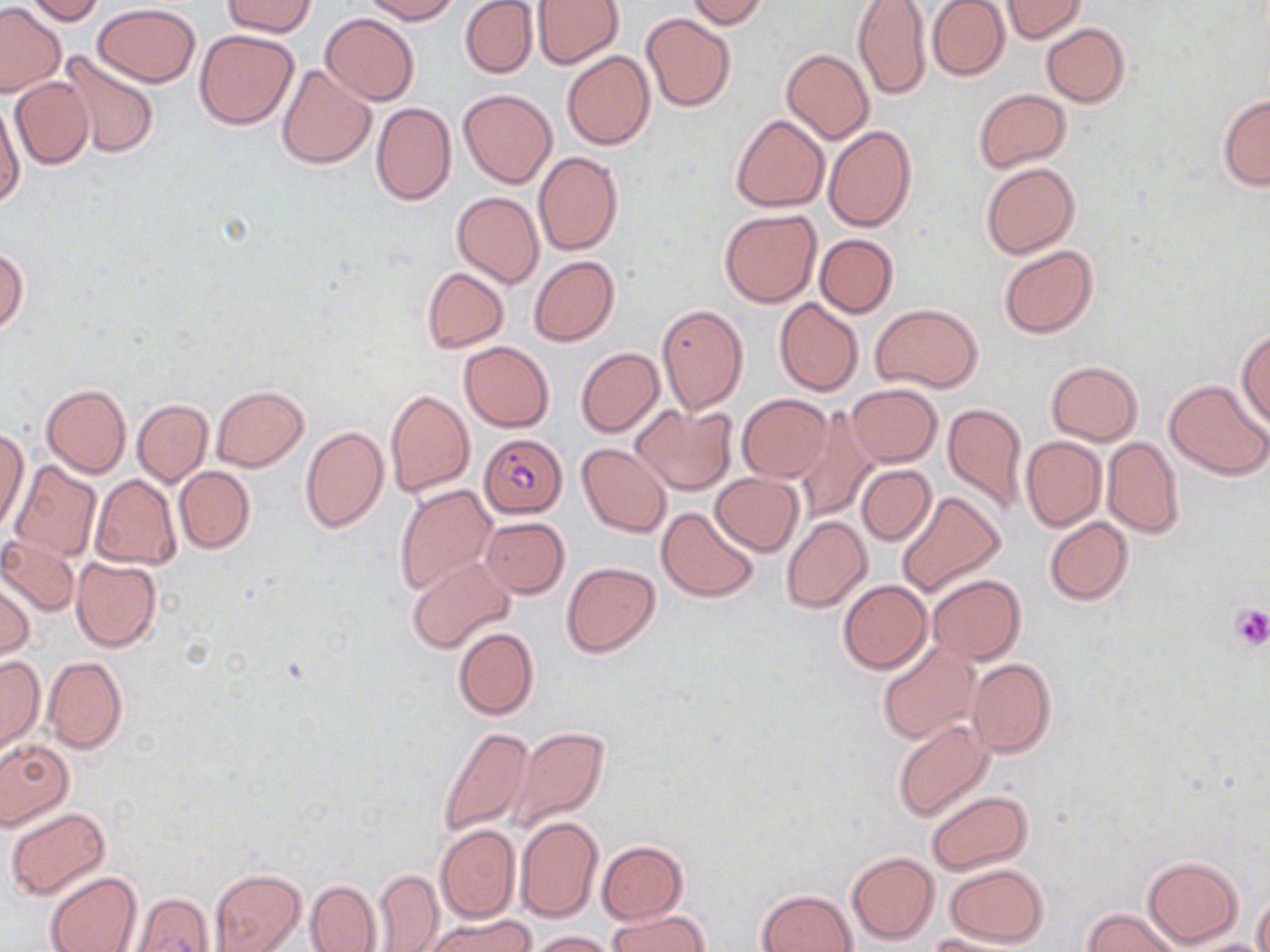

slide-level diagnosis = Plasmodium falciparum
preparation = thin blood smear
Plasmodium falciparum-infected red blood cell locations = approximate bounding boxes as (x1, y1, x2, y2) in pixels: (481, 432, 567, 519)
uninfected red blood cell locations = approximate bounding boxes as (x1, y1, x2, y2) in pixels: (24, 0, 107, 25), (222, 0, 317, 37), (359, 0, 460, 23), (459, 0, 539, 79), (684, 0, 769, 28), (926, 0, 1009, 82), (533, 1, 623, 68), (852, 1, 932, 101), (999, 1, 1087, 42), (92, 3, 201, 86), (0, 4, 65, 96), (321, 13, 419, 105), (642, 13, 736, 111), (1041, 22, 1129, 107), (194, 29, 299, 130), (781, 48, 874, 143), (56, 49, 162, 158), (561, 50, 655, 150), (276, 63, 376, 169), (10, 76, 93, 169), (457, 88, 556, 189), (974, 88, 1070, 171), (0, 94, 24, 211), (1218, 94, 1270, 192), (371, 102, 456, 206), (731, 114, 829, 212), (823, 126, 916, 232), (533, 151, 622, 255), (980, 162, 1080, 259), (452, 191, 544, 289), (720, 209, 821, 307), (815, 234, 898, 318), (999, 245, 1097, 338), (0, 249, 27, 335), (528, 255, 619, 346), (421, 267, 509, 353), (774, 298, 863, 396), (656, 303, 749, 415), (871, 303, 984, 391), (1237, 329, 1270, 429), (458, 340, 554, 431), (575, 348, 664, 437), (1045, 361, 1142, 445), (1165, 379, 1269, 479), (41, 383, 131, 479), (846, 383, 942, 466), (211, 386, 308, 471), (386, 388, 474, 497), (737, 393, 831, 482), (132, 399, 212, 486), (634, 402, 737, 495), (942, 402, 1028, 515), (794, 407, 877, 522), (301, 426, 388, 534), (0, 430, 29, 534), (1021, 436, 1106, 532), (1102, 437, 1183, 538), (577, 442, 671, 537), (10, 461, 103, 563), (855, 465, 935, 545), (174, 466, 255, 554), (711, 472, 804, 555), (90, 474, 181, 569), (393, 484, 494, 594), (895, 489, 1007, 599), (657, 507, 759, 601), (480, 516, 569, 597), (782, 516, 872, 613), (1044, 517, 1134, 605), (0, 533, 80, 616), (406, 555, 515, 652), (71, 557, 163, 653), (561, 561, 659, 657), (928, 574, 1025, 665), (1, 576, 33, 660), (838, 580, 931, 673), (452, 627, 539, 720), (876, 641, 980, 745), (0, 656, 43, 753), (43, 656, 127, 752), (967, 658, 1056, 757), (892, 719, 995, 821), (437, 725, 536, 837), (508, 726, 611, 832), (0, 738, 73, 829), (926, 790, 1033, 874), (6, 808, 110, 900), (515, 815, 602, 924), (435, 824, 521, 923), (597, 840, 687, 923), (847, 851, 939, 945), (1143, 855, 1243, 947), (943, 863, 1049, 947), (209, 868, 305, 951), (373, 869, 445, 950), (45, 872, 141, 952), (306, 879, 380, 952), (758, 888, 857, 952), (130, 892, 213, 952), (1253, 893, 1270, 952), (1083, 907, 1183, 952), (608, 909, 710, 952), (426, 914, 535, 952), (528, 930, 620, 951), (922, 933, 1026, 951), (1186, 939, 1269, 952)
stain = May-Grünwald-Giemsa
field of view = one of a larger specimen
image size = 1270×952 pixels
magnification = 1000x
modality = light microscopy
platelet locations = approximate bounding boxes as (x1, y1, x2, y2) in pixels: (1229, 604, 1270, 652)